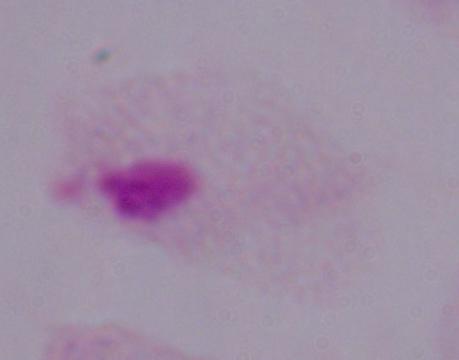

A trichomonad is seen. Captured at 1000x magnification. Photomicrograph.